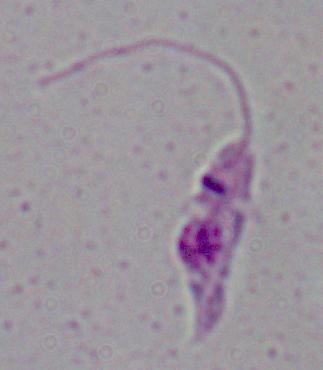

Summary:
  - Identification: Leishmania
  - Modality: micrograph
  - Magnification: 1000x